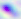 Toxoplasma gondii is seen. 400x magnification. Photomicrograph.